Evaluate for malaria.
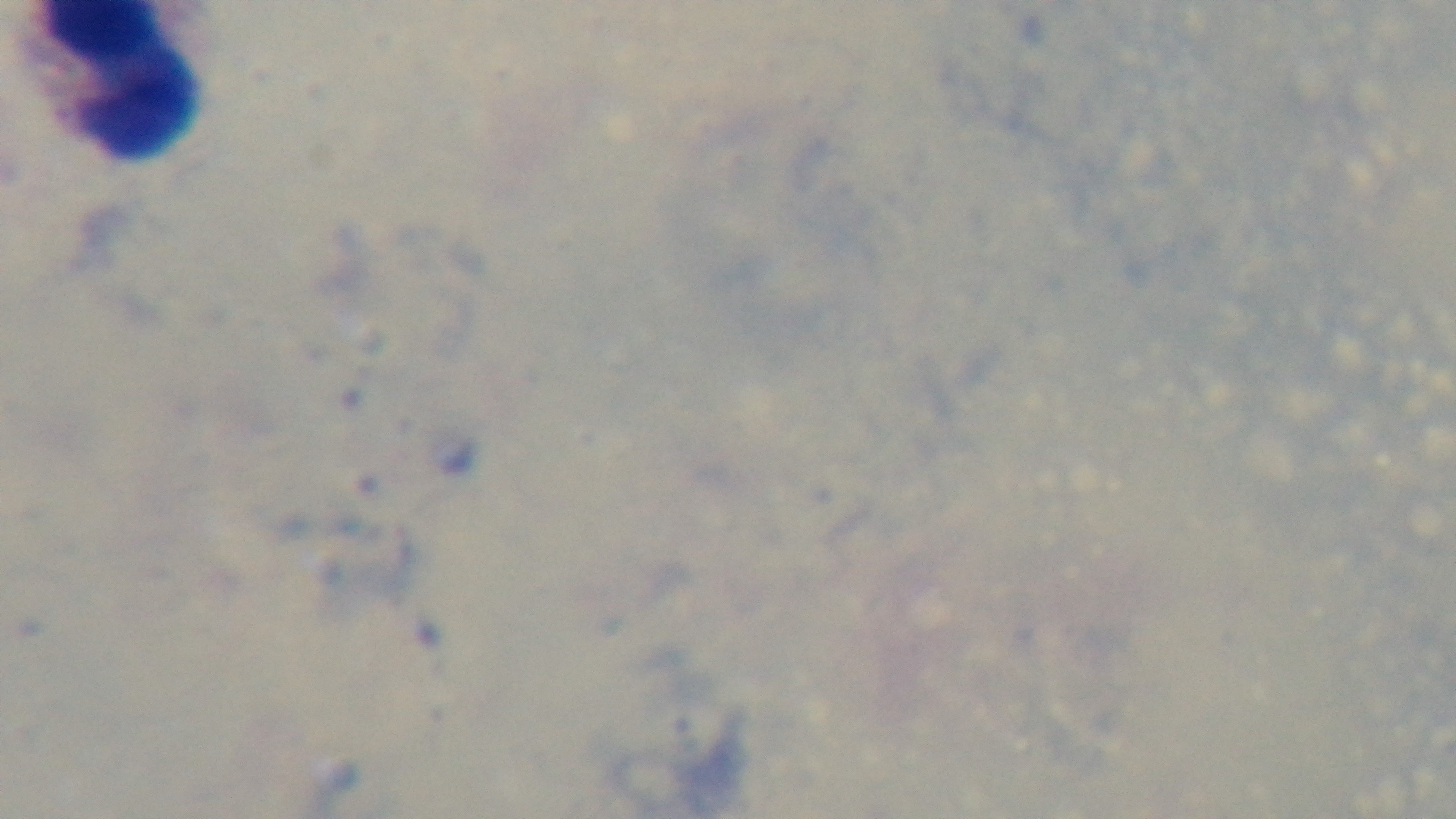

It is uninfected.

Summary:
  - Capture: mounted 4K digital camera
  - Stain: Giemsa
  - Modality: light microscopy
  - Preparation: thick smear
  - Objective: 100x oil immersion
  - Field of view: one from the slide